Locate every Plasmodium ovale-infected red blood cell.
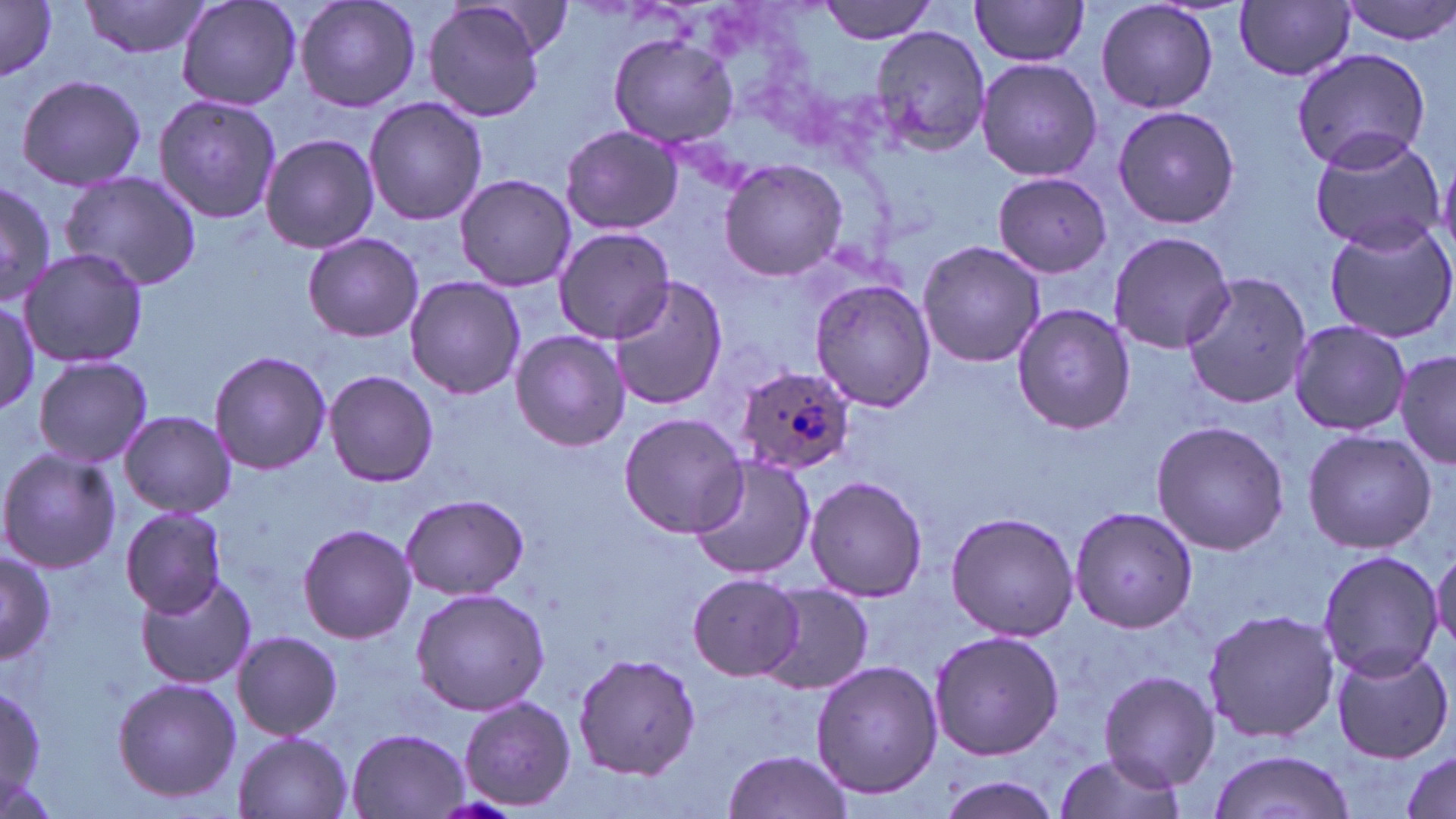

Approximate bounding boxes as named x1/y1/x2/y2 corners in pixels.
Plasmodium ovale-infected red blood cells: (x1=733, y1=363, x2=855, y2=473).

Summary:
  - Uninfected red blood cell locations: (x1=79, y1=0, x2=213, y2=59), (x1=176, y1=0, x2=302, y2=112), (x1=295, y1=0, x2=421, y2=114), (x1=816, y1=0, x2=943, y2=43), (x1=968, y1=0, x2=1092, y2=67), (x1=1093, y1=0, x2=1220, y2=114), (x1=1341, y1=0, x2=1456, y2=46), (x1=1236, y1=2, x2=1355, y2=81), (x1=0, y1=3, x2=59, y2=80), (x1=423, y1=3, x2=550, y2=121), (x1=869, y1=24, x2=991, y2=154), (x1=610, y1=29, x2=739, y2=149), (x1=1291, y1=47, x2=1432, y2=173), (x1=976, y1=58, x2=1101, y2=182), (x1=14, y1=73, x2=149, y2=191), (x1=153, y1=94, x2=282, y2=225), (x1=364, y1=96, x2=487, y2=226), (x1=1110, y1=103, x2=1241, y2=229), (x1=561, y1=124, x2=680, y2=235), (x1=1307, y1=128, x2=1444, y2=255), (x1=259, y1=132, x2=380, y2=255), (x1=718, y1=158, x2=850, y2=281), (x1=59, y1=169, x2=202, y2=292), (x1=991, y1=172, x2=1113, y2=277), (x1=453, y1=173, x2=578, y2=292), (x1=0, y1=181, x2=58, y2=309), (x1=1323, y1=220, x2=1456, y2=343), (x1=552, y1=226, x2=674, y2=343), (x1=303, y1=231, x2=423, y2=343), (x1=1108, y1=231, x2=1235, y2=354), (x1=917, y1=239, x2=1045, y2=368), (x1=20, y1=247, x2=150, y2=370), (x1=1182, y1=268, x2=1314, y2=408), (x1=405, y1=276, x2=523, y2=397), (x1=609, y1=277, x2=729, y2=412), (x1=808, y1=278, x2=934, y2=411), (x1=1, y1=293, x2=40, y2=417), (x1=1010, y1=302, x2=1139, y2=435), (x1=1287, y1=320, x2=1412, y2=437), (x1=510, y1=329, x2=629, y2=452), (x1=208, y1=349, x2=332, y2=476), (x1=1395, y1=350, x2=1456, y2=468), (x1=32, y1=355, x2=153, y2=468), (x1=324, y1=370, x2=439, y2=488), (x1=119, y1=410, x2=235, y2=518), (x1=618, y1=412, x2=746, y2=537), (x1=1149, y1=420, x2=1288, y2=556), (x1=1301, y1=428, x2=1436, y2=555), (x1=0, y1=448, x2=120, y2=574), (x1=688, y1=456, x2=814, y2=581), (x1=805, y1=474, x2=927, y2=602), (x1=400, y1=493, x2=529, y2=600), (x1=1070, y1=505, x2=1200, y2=634), (x1=120, y1=506, x2=228, y2=617), (x1=950, y1=516, x2=1080, y2=643), (x1=296, y1=523, x2=416, y2=643), (x1=1430, y1=545, x2=1456, y2=658), (x1=0, y1=548, x2=55, y2=667), (x1=1315, y1=550, x2=1443, y2=681), (x1=134, y1=573, x2=259, y2=692), (x1=688, y1=574, x2=804, y2=679), (x1=761, y1=585, x2=873, y2=694), (x1=409, y1=587, x2=552, y2=717), (x1=1203, y1=606, x2=1340, y2=742), (x1=928, y1=629, x2=1064, y2=761), (x1=231, y1=630, x2=345, y2=741), (x1=1330, y1=647, x2=1453, y2=764), (x1=573, y1=649, x2=700, y2=782), (x1=810, y1=660, x2=944, y2=800), (x1=1098, y1=670, x2=1218, y2=789), (x1=111, y1=676, x2=241, y2=806), (x1=0, y1=683, x2=47, y2=800), (x1=458, y1=694, x2=577, y2=811), (x1=345, y1=728, x2=470, y2=819), (x1=233, y1=732, x2=354, y2=819), (x1=1209, y1=747, x2=1355, y2=819), (x1=719, y1=750, x2=855, y2=818), (x1=1048, y1=750, x2=1190, y2=819), (x1=1398, y1=750, x2=1454, y2=817), (x1=932, y1=774, x2=1065, y2=818)
  - Slide-level diagnosis: Plasmodium ovale
  - Stain: May-Grünwald-Giemsa
  - Preparation: thin blood smear
  - Magnification: 1000x
  - Field of view: single
  - Image size: 1456×819 pixels
  - Modality: light microscopy